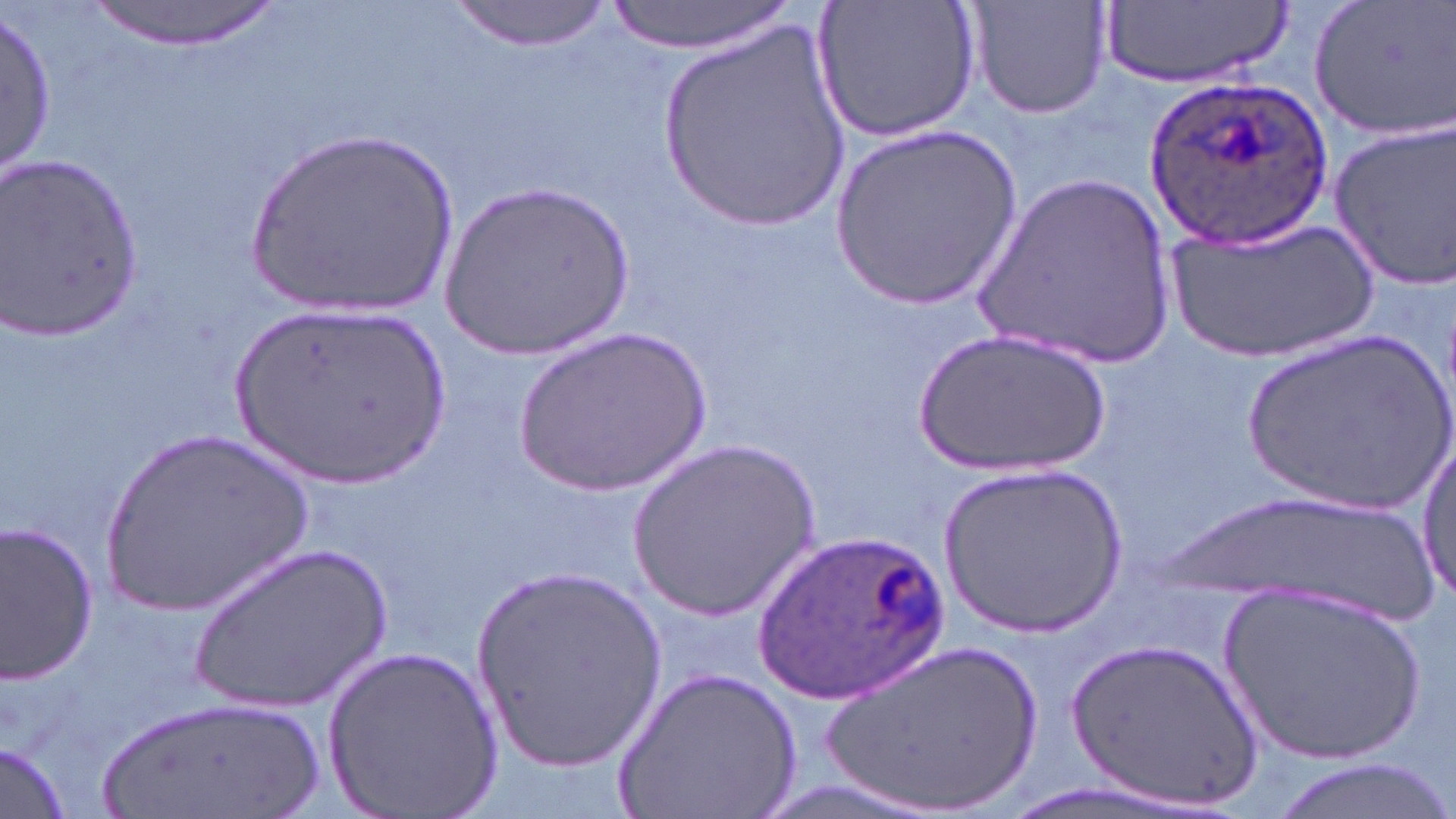

Summary:
  - Coordinate format: approximate bounding boxes as named x1/y1/x2/y2 corners in pixels
  - Uninfected red blood cell locations: (x1=606, y1=0, x2=792, y2=54), (x1=813, y1=0, x2=982, y2=143), (x1=964, y1=0, x2=1115, y2=120), (x1=1102, y1=0, x2=1291, y2=86), (x1=1308, y1=0, x2=1456, y2=140), (x1=81, y1=1, x2=283, y2=50), (x1=446, y1=1, x2=615, y2=51), (x1=0, y1=9, x2=54, y2=185), (x1=658, y1=20, x2=852, y2=229), (x1=1329, y1=123, x2=1456, y2=288), (x1=242, y1=124, x2=463, y2=321), (x1=832, y1=124, x2=1023, y2=310), (x1=2, y1=153, x2=148, y2=342), (x1=970, y1=174, x2=1177, y2=370), (x1=439, y1=183, x2=634, y2=361), (x1=1163, y1=216, x2=1377, y2=365), (x1=232, y1=304, x2=449, y2=487), (x1=511, y1=327, x2=712, y2=497), (x1=915, y1=329, x2=1108, y2=478), (x1=1241, y1=329, x2=1456, y2=521), (x1=95, y1=430, x2=317, y2=614), (x1=627, y1=440, x2=821, y2=621), (x1=1413, y1=440, x2=1456, y2=605), (x1=939, y1=461, x2=1132, y2=637), (x1=0, y1=519, x2=99, y2=682), (x1=186, y1=543, x2=393, y2=713), (x1=470, y1=568, x2=667, y2=771), (x1=1218, y1=581, x2=1431, y2=770), (x1=1065, y1=632, x2=1265, y2=816), (x1=817, y1=635, x2=1052, y2=819), (x1=327, y1=643, x2=505, y2=818), (x1=613, y1=666, x2=803, y2=819), (x1=92, y1=692, x2=325, y2=819), (x1=1, y1=743, x2=72, y2=818)
  - Plasmodium ovale-infected red blood cell locations: (x1=1145, y1=72, x2=1332, y2=251), (x1=758, y1=526, x2=955, y2=704)
  - Slide-level diagnosis: Plasmodium ovale
  - Magnification: 1000x
  - Preparation: thin blood smear
  - Field of view: single
  - Stain: May-Grünwald-Giemsa
  - Modality: optical microscopy
  - Image size: 1456×819 pixels